Locate every leukocyte (white blood cell).
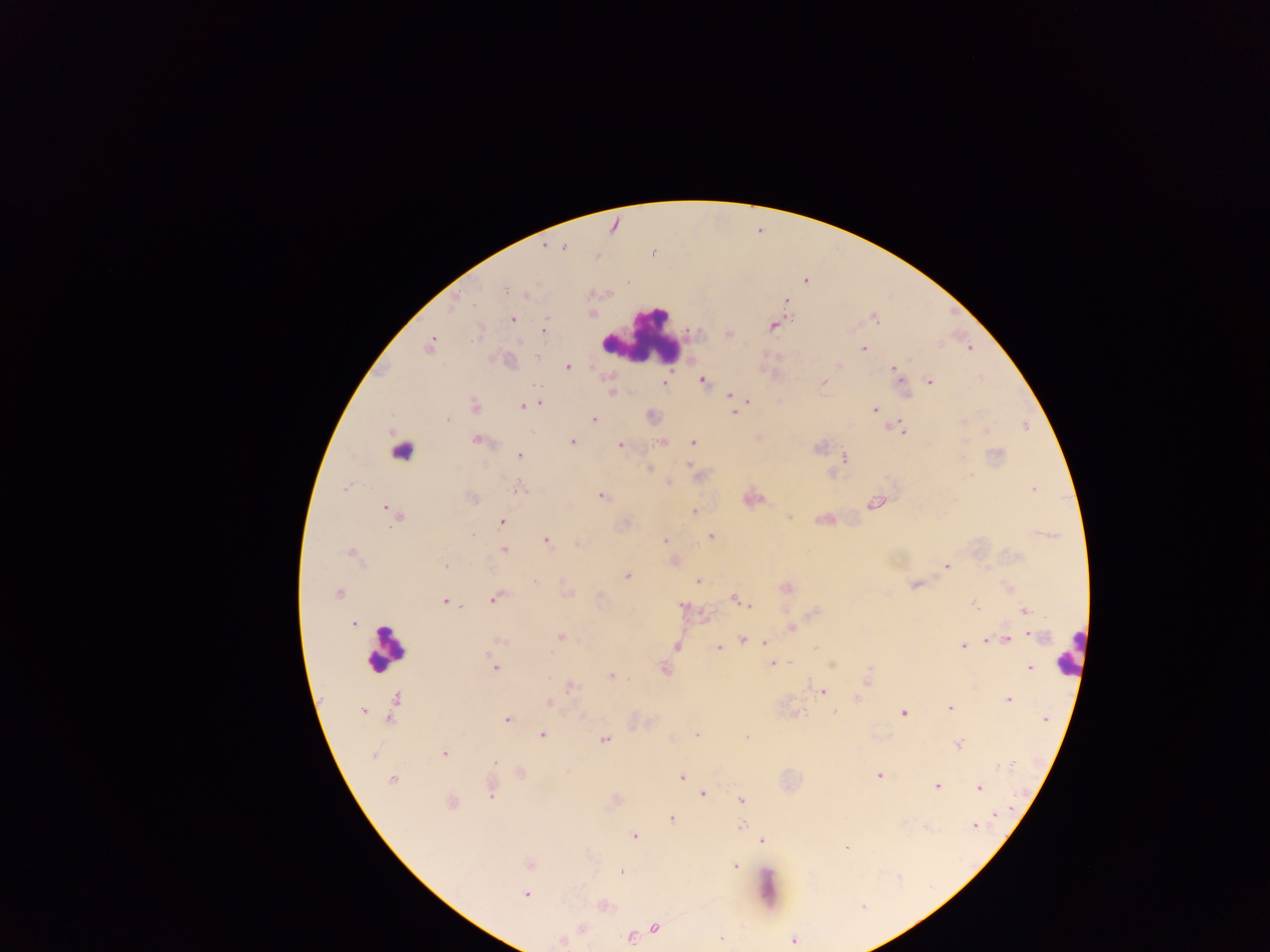

Approximate centers as [x, y] in pixels.
Leukocytes: [643, 337], [404, 446], [384, 648], [1069, 652].

Malaria parasite locations: [551, 245], [563, 246], [653, 253], [504, 289], [528, 294], [786, 301], [512, 319], [874, 319], [773, 325], [545, 331], [729, 334], [521, 342], [430, 346], [863, 349], [538, 357], [838, 366], [567, 367], [895, 369], [703, 380], [930, 381], [824, 382], [664, 383], [611, 393], [730, 395], [749, 401], [539, 403], [523, 406], [474, 407], [874, 409], [734, 412], [594, 419], [446, 420], [962, 422], [900, 429], [987, 430], [477, 440], [572, 442], [663, 442], [693, 443], [620, 445], [997, 454], [519, 455], [963, 455], [844, 458], [689, 465], [650, 469], [669, 482], [519, 488], [346, 489], [1034, 489], [603, 496], [472, 498], [873, 503], [388, 511], [695, 511], [395, 515], [789, 517], [502, 522], [471, 535], [711, 536], [664, 540], [547, 541], [577, 544], [504, 549], [352, 555], [445, 565], [946, 566], [627, 576], [699, 580], [534, 582], [915, 584], [787, 587], [338, 593], [600, 596], [494, 599], [736, 599], [445, 602], [973, 603], [748, 605], [683, 606], [1026, 611], [353, 625], [792, 628], [1036, 636], [560, 637], [990, 639], [742, 640], [1005, 640], [500, 642], [764, 643], [962, 645], [676, 646], [719, 648], [815, 648], [773, 663], [495, 668], [1029, 668], [665, 670], [611, 676], [867, 681], [571, 686], [822, 692], [856, 699], [1008, 699], [548, 703], [950, 707], [363, 712], [835, 713], [903, 713], [795, 714], [1045, 719], [507, 720], [542, 735], [696, 735], [746, 736], [604, 739], [958, 745], [444, 754], [373, 755], [494, 762], [1008, 766], [878, 776], [682, 777], [393, 779], [937, 786], [979, 787], [491, 793], [703, 794], [741, 801], [451, 802], [995, 814], [672, 818], [741, 826], [975, 826], [634, 836], [763, 840], [846, 848], [529, 864], [735, 865], [621, 872], [526, 895], [862, 907], [655, 928], [630, 937], [722, 938], [793, 940], [560, 941]. Sample from Ghana. Photographed through a microscope with a mobile-phone camera. Image is 1270×952 pixels. One field of view. Thick blood film.